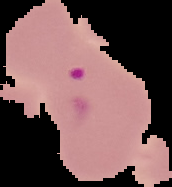

result = Plasmodium parasites detected
image size = 172×187 pixels
preparation = thin blood film
image type = cell region segmented out of the field of view; surrounding area masked to black